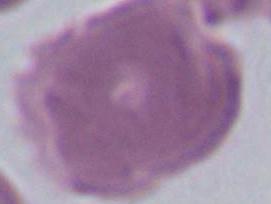
Summary:
  - Identification: red blood cell
  - Modality: photomicrograph
  - Magnification: 1000x